Assess this cell for malaria.
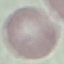
It is uninfected.

Thin smear of blood. Giemsa stain. Cell patch, automatically extracted from a larger field of view and resized to 64 × 64 pixels. Acquired by smartphone through the microscope eyepiece.